Comment on the morphology of the erythrocytes.
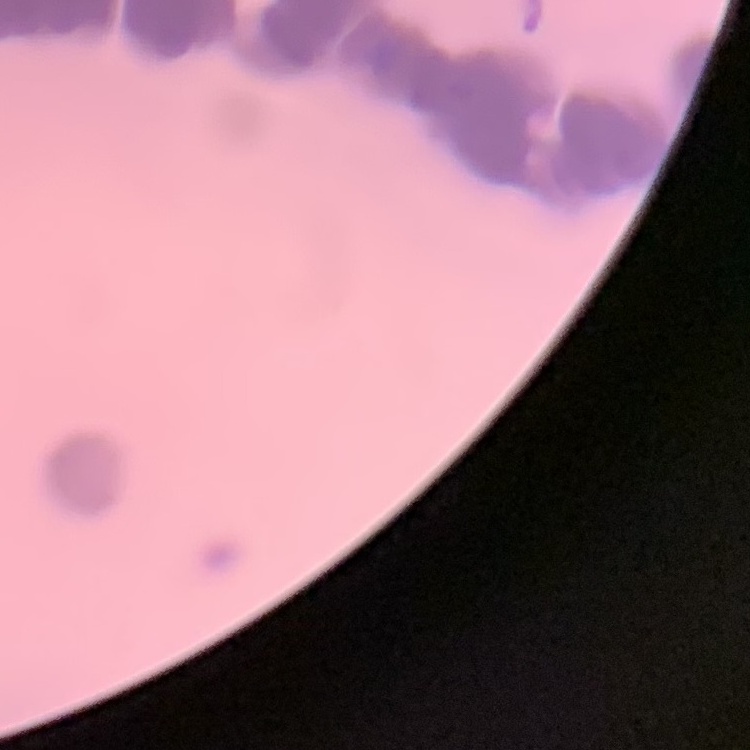
They show rouleaux formation.

One tile cut from a larger photomicrograph. Thin blood smear. Field's or Giemsa stain.